Classify this cell by malaria status.
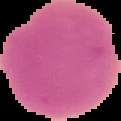
Uninfected.

image size = 121×121 pixels
image type = segmented cell region on a black background
preparation = thin blood film